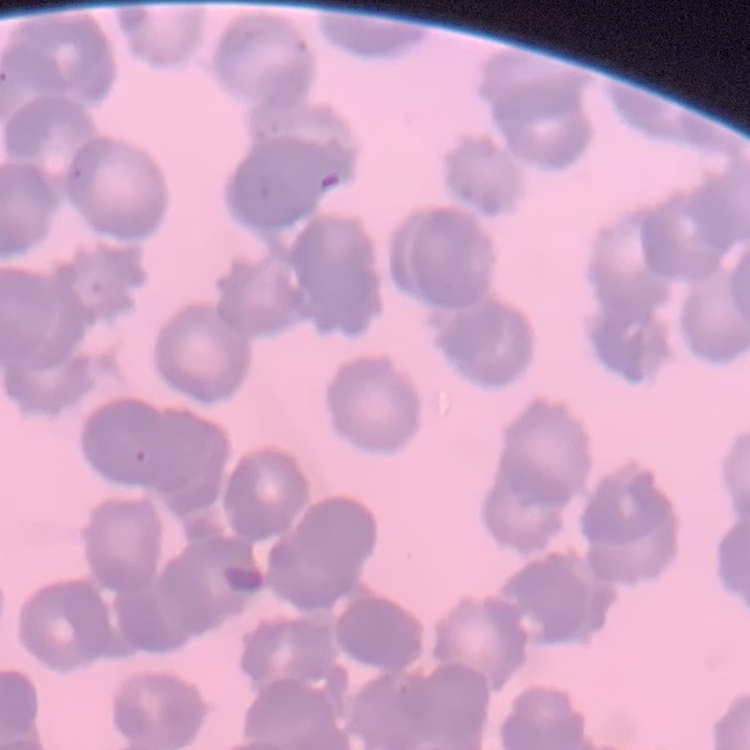

The red blood cells exhibit rouleaux formation. Square crop of a larger photomicrograph. Thin blood film. Field's or Giemsa stain.